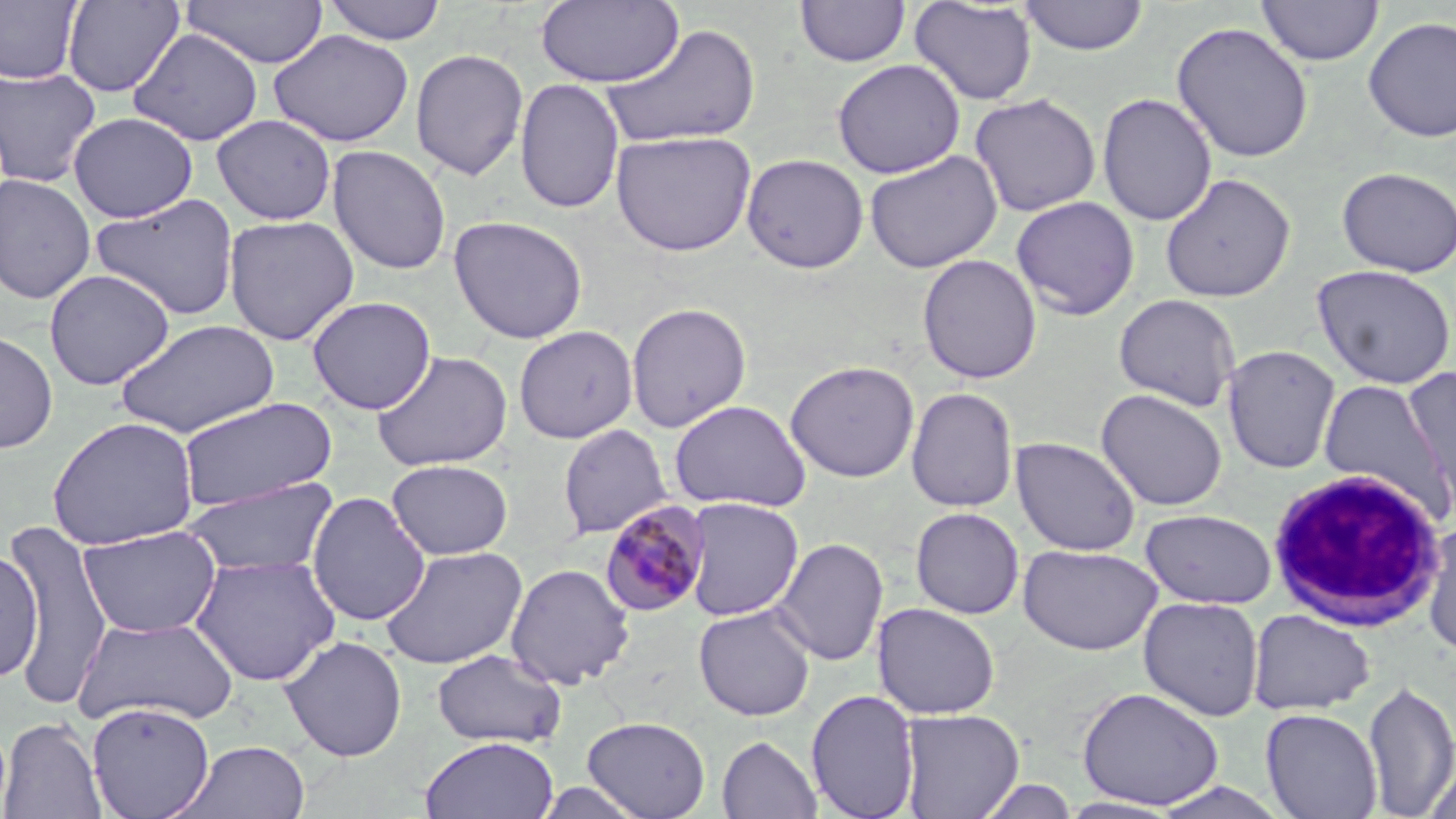
{
  "slide_level_diagnosis": "Plasmodium malariae",
  "stain": "May-Grünwald-Giemsa",
  "white_blood_cell_locations": "approximate bounding boxes as [x1, y1, x2, y2] in pixels: [1266, 468, 1446, 631]",
  "preparation": "thin blood film",
  "uninfected_red_blood_cell_locations": "approximate bounding boxes as [x1, y1, x2, y2] in pixels: [0, 0, 82, 85], [62, 0, 184, 97], [180, 0, 329, 68], [321, 0, 447, 45], [796, 0, 910, 67], [909, 0, 1037, 105], [1018, 0, 1148, 56], [1256, 0, 1383, 66], [536, 1, 684, 87], [1362, 15, 1456, 143], [1171, 21, 1314, 163], [602, 23, 761, 149], [129, 28, 265, 146], [270, 29, 413, 147], [410, 48, 529, 181], [832, 59, 966, 178], [0, 66, 102, 188], [515, 77, 625, 214], [1097, 92, 1217, 226], [969, 93, 1101, 217], [68, 112, 198, 223], [211, 114, 337, 225], [611, 130, 757, 256], [327, 145, 451, 275], [864, 150, 1002, 273], [741, 153, 869, 273], [1336, 166, 1456, 278], [0, 173, 96, 304], [1160, 173, 1296, 303], [90, 192, 240, 322], [1011, 196, 1140, 320], [223, 214, 360, 346], [448, 215, 588, 344], [917, 253, 1041, 384], [1311, 263, 1455, 390], [43, 269, 175, 390], [1113, 293, 1241, 412], [307, 296, 436, 415], [625, 302, 751, 433], [115, 319, 280, 438], [513, 325, 638, 443], [0, 330, 58, 454], [1222, 344, 1341, 474], [370, 350, 513, 472], [785, 360, 920, 482], [1401, 367, 1456, 516], [1318, 377, 1452, 520], [906, 387, 1018, 513], [1095, 387, 1228, 511], [177, 397, 338, 512], [669, 400, 812, 512], [46, 416, 200, 551], [557, 423, 673, 539], [1010, 436, 1142, 556], [386, 459, 513, 560], [180, 477, 340, 579], [306, 491, 431, 627], [682, 497, 804, 621], [910, 507, 1025, 619], [1140, 509, 1277, 609], [4, 517, 113, 710], [1421, 521, 1456, 657], [77, 525, 222, 638], [772, 537, 889, 666], [0, 542, 42, 686], [1017, 543, 1163, 656], [379, 545, 528, 671], [189, 553, 341, 687], [505, 562, 635, 690], [1138, 596, 1264, 721], [872, 602, 1000, 719], [693, 604, 815, 721], [1247, 609, 1375, 714], [73, 615, 239, 728], [279, 635, 408, 762], [432, 648, 567, 750], [1362, 678, 1456, 817], [1077, 686, 1224, 809], [805, 688, 921, 819], [86, 701, 215, 819], [898, 708, 1024, 819], [1260, 708, 1383, 818], [582, 715, 712, 818], [1, 716, 106, 818], [419, 735, 560, 819], [716, 735, 823, 819], [173, 740, 311, 818], [1422, 755, 1456, 819], [974, 777, 1078, 818], [1147, 781, 1293, 819]",
  "plasmodium_malariae_infected_red_blood_cell_locations": "approximate bounding boxes as [x1, y1, x2, y2] in pixels: [600, 501, 711, 616]",
  "modality": "optical microscopy",
  "magnification": "1000x",
  "field_of_view": "single",
  "image_size": "1456×819 pixels"
}